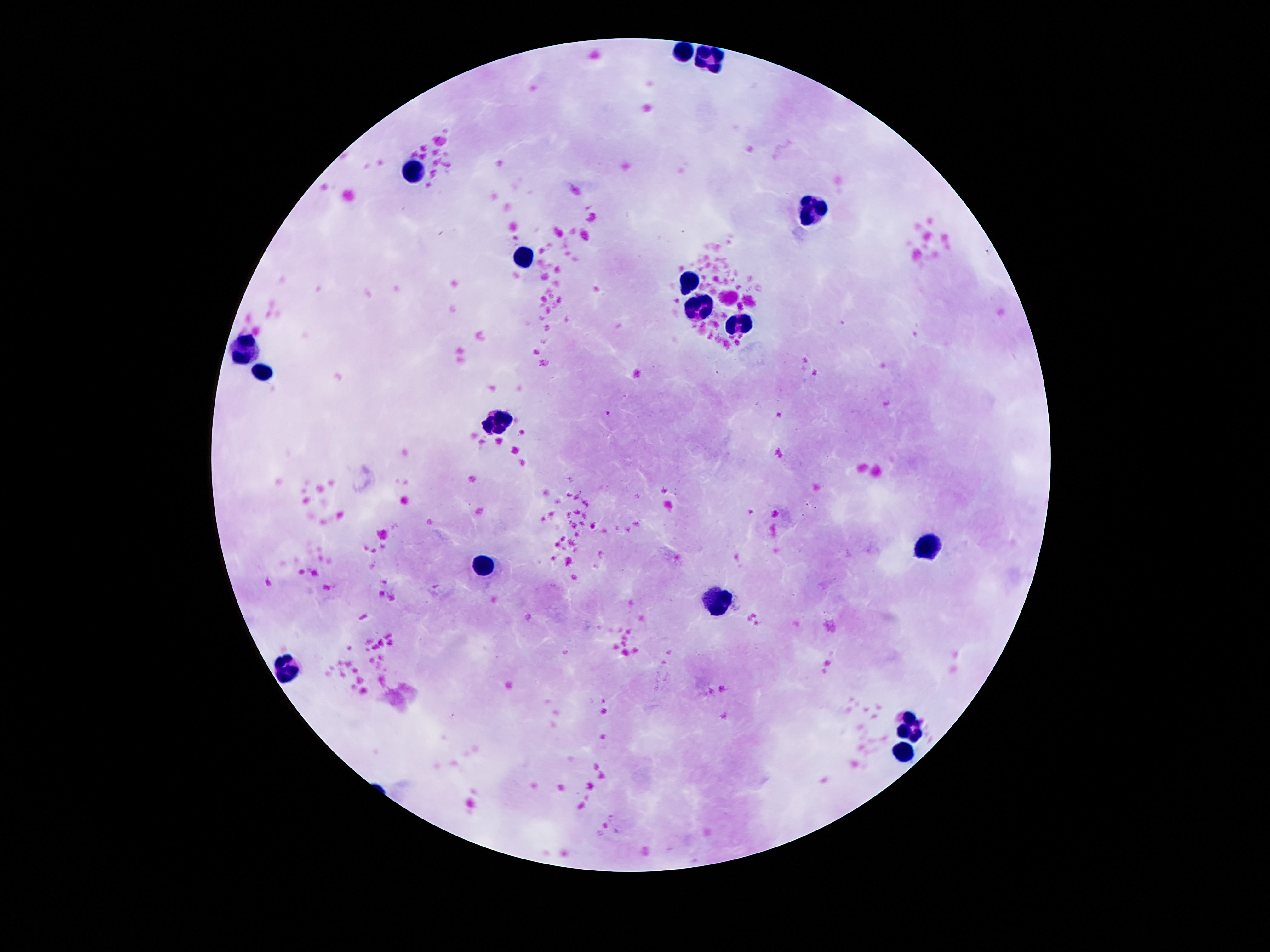
Approximate centers as [x, y] in pixels. Leukocyte locations: [685, 48], [707, 59], [414, 168], [810, 208], [523, 258], [691, 283], [697, 305], [736, 327], [244, 348], [263, 373], [496, 421], [927, 548], [483, 565], [716, 607], [286, 669], [915, 724], [903, 751]. Thick blood film. Image is 1270×952 pixels. One field from this slide. Patient malaria status: uninfected. Smartphone photograph taken through the microscope eyepiece. 100x magnification. Giemsa-stained preparation.